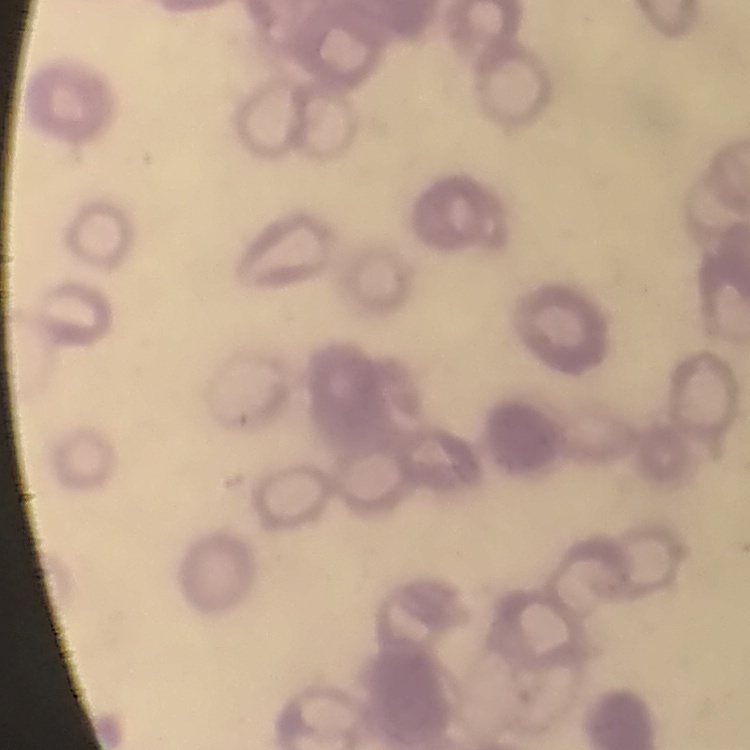

The erythrocytes exhibit rouleaux formation. Thin blood smear. Stained with either Field's or Giemsa. One tile cut from a larger photomicrograph.